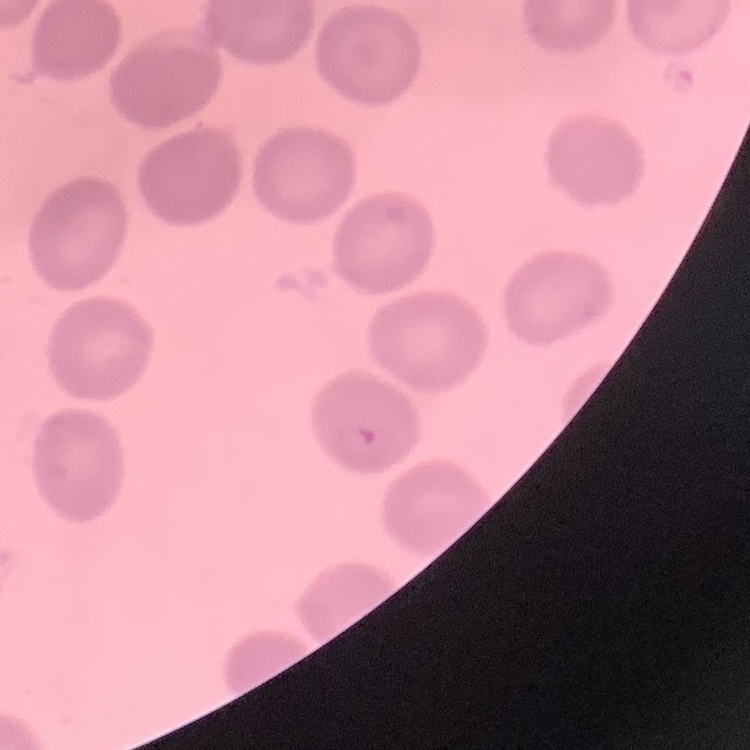
red blood cell morphology = no rouleaux formation
image type = one tile cut from a larger photomicrograph
stain = Field's or Giemsa
preparation = thin peripheral smear